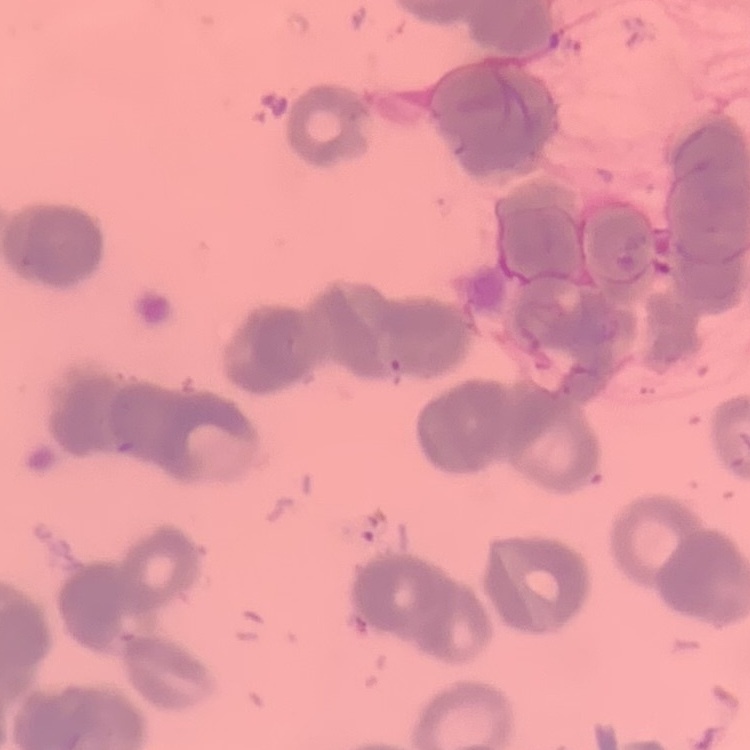
Summary:
  - Erythrocyte morphology: rouleaux formation
  - Image type: one tile cut from a larger photomicrograph
  - Preparation: thin blood smear
  - Stain: Field's or Giemsa